Assess this cell for malaria.
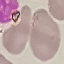
It is uninfected.

capture = smartphone through the microscope eyepiece
stain = Giemsa
preparation = thin blood film
image type = automatically extracted cell patch, resized to 64 × 64 pixels